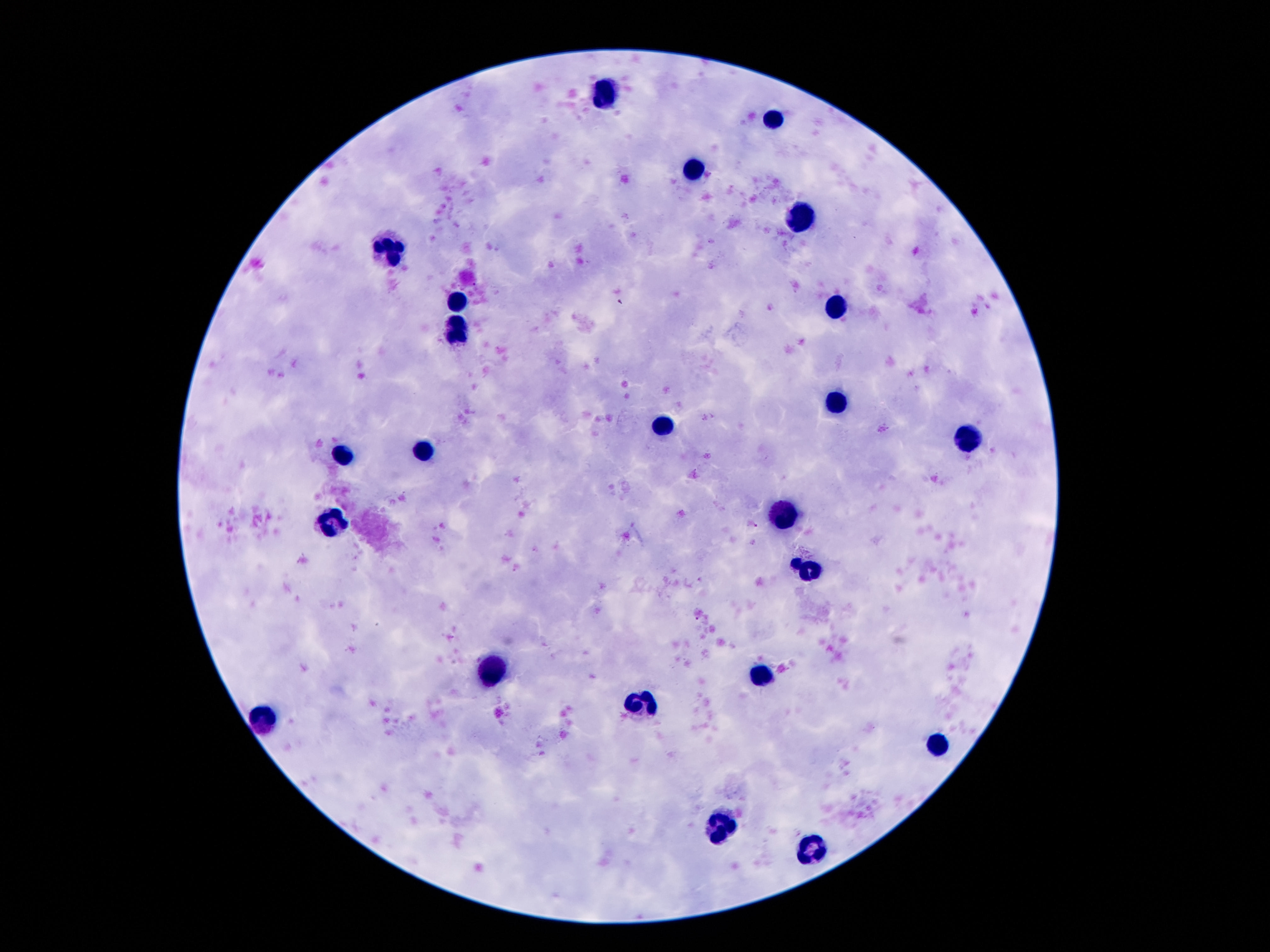

Approximate centers as (x, y) in pixels. Leukocyte locations: (603, 94), (773, 118), (694, 173), (802, 217), (387, 249), (457, 303), (838, 305), (457, 329), (833, 401), (663, 425), (965, 440), (423, 447), (342, 451), (783, 518), (332, 521), (490, 672), (757, 677), (641, 706), (265, 720), (937, 744), (716, 826), (814, 850). Image is 1270×952 pixels. Giemsa-stained preparation. Smartphone photograph taken through the microscope eyepiece. Thick blood film. Patient malaria status: not infected. One field from this slide. 100x magnification.